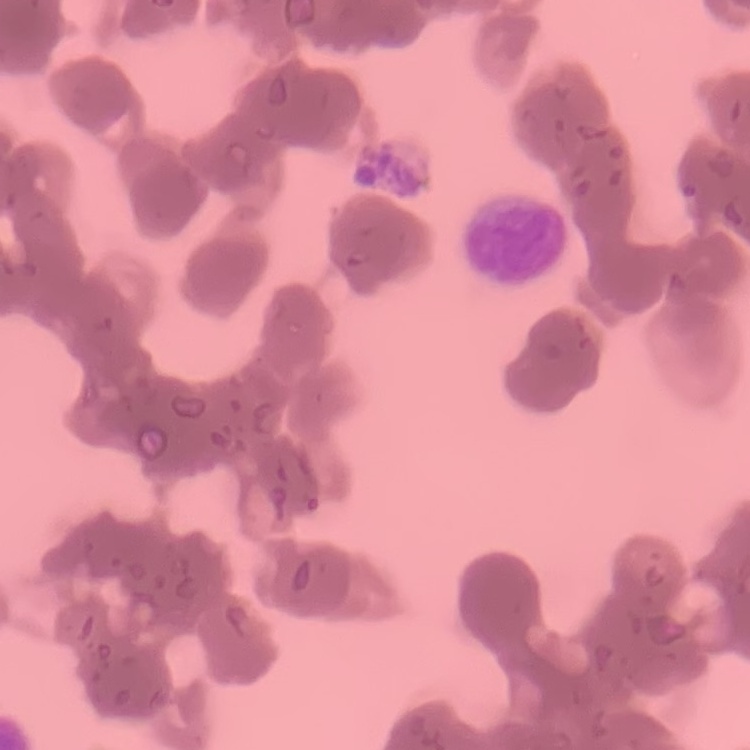
erythrocyte morphology = rouleaux formation
stain = Field's or Giemsa
image type = square crop of a larger photomicrograph
preparation = thin blood film